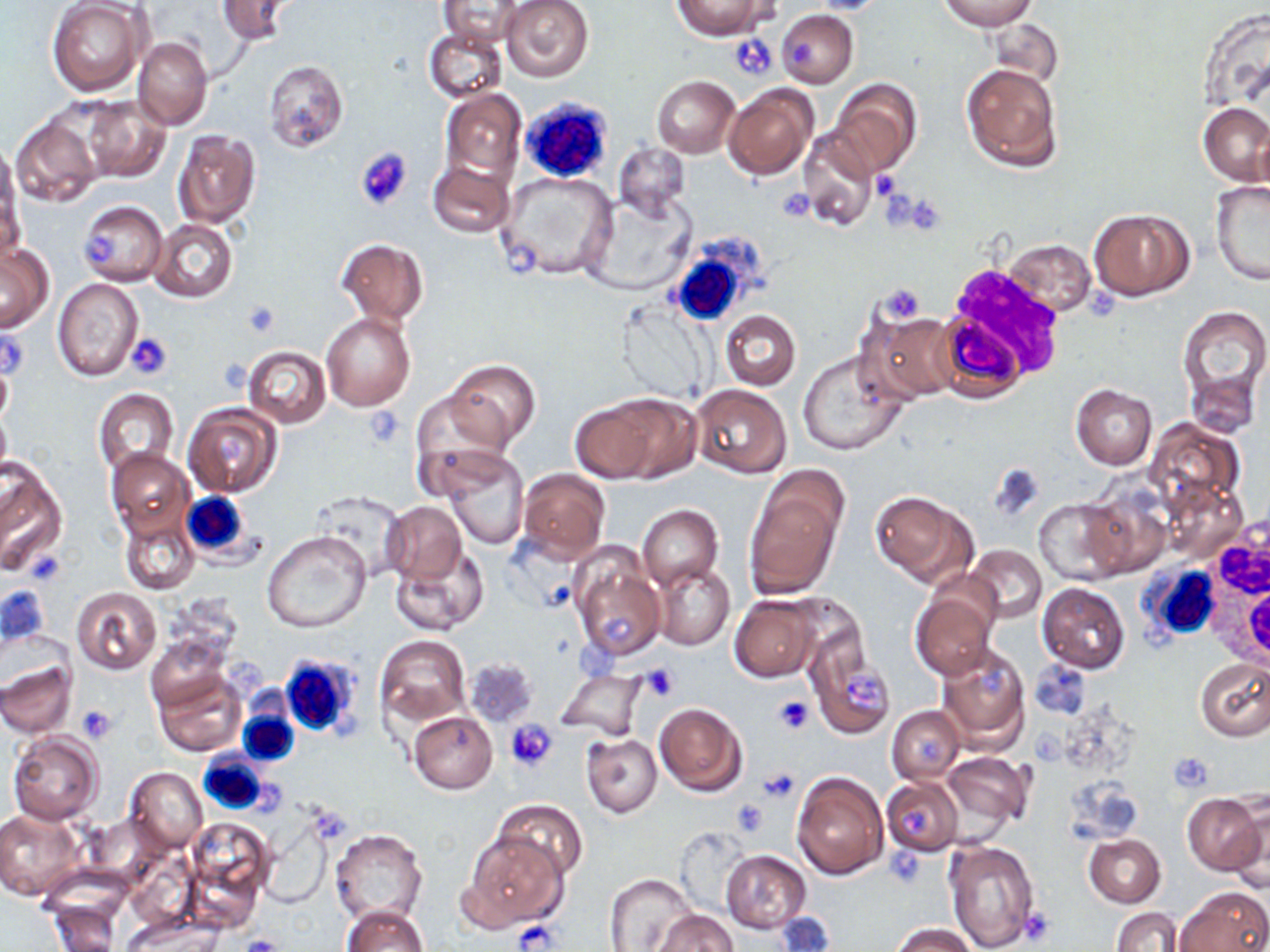
{
  "slide_level_diagnosis": "no evidence of blood parasites",
  "uninfected_red_blood_cell_locations": "approximate bounding boxes as [x1, y1, x2, y2] in pixels: [216, 0, 298, 44], [438, 0, 529, 48], [500, 0, 594, 83], [673, 0, 771, 39], [938, 0, 1036, 30], [805, 1, 896, 15], [47, 2, 149, 96], [776, 10, 858, 88], [987, 17, 1063, 88], [423, 28, 508, 102], [132, 38, 212, 129], [263, 60, 348, 152], [962, 63, 1062, 173], [651, 75, 739, 158], [831, 79, 921, 175], [723, 84, 817, 180], [439, 88, 527, 185], [77, 95, 170, 184], [1199, 104, 1270, 186], [10, 113, 102, 210], [796, 125, 879, 231], [171, 129, 260, 228], [0, 138, 19, 232], [613, 143, 691, 221], [428, 161, 514, 238], [497, 172, 619, 282], [1210, 180, 1270, 286], [1, 183, 24, 267], [583, 193, 695, 296], [78, 201, 166, 285], [1089, 208, 1193, 301], [148, 218, 238, 303], [337, 239, 428, 325], [1003, 239, 1097, 316], [1, 242, 54, 332], [52, 277, 143, 382], [615, 301, 714, 404], [1178, 305, 1270, 412], [860, 309, 964, 403], [321, 311, 416, 412], [719, 311, 800, 389], [242, 345, 330, 428], [797, 351, 908, 456], [0, 358, 12, 431], [444, 359, 539, 449], [1070, 383, 1156, 469], [690, 385, 792, 479], [92, 389, 179, 475], [409, 392, 511, 497], [571, 394, 679, 484], [183, 402, 282, 498], [0, 409, 11, 476], [1146, 416, 1245, 513], [106, 448, 195, 541], [438, 448, 531, 549], [0, 464, 65, 575], [519, 468, 611, 560], [745, 477, 846, 598], [1159, 479, 1247, 566], [1081, 486, 1173, 580], [870, 491, 977, 588], [1034, 496, 1129, 586], [383, 502, 465, 584], [637, 504, 722, 592], [118, 506, 200, 596], [261, 530, 371, 634], [965, 545, 1047, 623], [391, 547, 490, 635], [571, 553, 665, 659], [652, 562, 734, 650], [1037, 583, 1130, 672], [71, 587, 161, 674], [911, 587, 997, 678], [729, 596, 820, 681], [374, 635, 470, 726], [804, 639, 896, 739], [935, 644, 1030, 754], [1196, 658, 1270, 740], [465, 659, 538, 726], [1029, 659, 1091, 719], [0, 663, 76, 739], [150, 666, 248, 758], [556, 668, 647, 740], [655, 703, 746, 796], [886, 706, 964, 784], [408, 711, 497, 793], [8, 732, 103, 825], [583, 734, 662, 817], [942, 751, 1035, 829], [124, 768, 208, 853], [792, 770, 888, 878], [881, 777, 963, 855], [1183, 792, 1267, 875], [493, 798, 588, 882], [1228, 801, 1270, 895], [0, 809, 85, 901], [259, 814, 333, 908], [184, 819, 274, 919], [331, 829, 427, 924], [460, 831, 564, 931], [1083, 833, 1164, 907], [943, 838, 1039, 952], [721, 850, 810, 933], [603, 873, 696, 952], [1176, 887, 1269, 952], [48, 902, 121, 951], [341, 904, 427, 952], [1111, 906, 1182, 952], [654, 910, 738, 952], [124, 913, 222, 951], [771, 913, 835, 952], [891, 922, 978, 952]",
  "modality": "optical microscopy",
  "stain": "May-Grünwald-Giemsa",
  "field_of_view": "one of a larger specimen",
  "platelet_locations": "approximate bounding boxes as [x1, y1, x2, y2] in pixels: [731, 34, 778, 80], [788, 34, 819, 70], [355, 146, 412, 212], [871, 171, 900, 201], [776, 188, 817, 220], [902, 194, 949, 235], [1084, 282, 1121, 321], [874, 285, 926, 325], [239, 300, 281, 338], [1, 328, 29, 381], [127, 332, 173, 380], [364, 408, 405, 448], [990, 465, 1044, 523], [24, 548, 66, 586], [597, 611, 635, 645], [574, 636, 619, 684], [975, 662, 1008, 700], [643, 666, 680, 701], [845, 674, 885, 707], [771, 695, 814, 736], [77, 706, 116, 742], [507, 719, 559, 771], [915, 733, 948, 764], [1168, 751, 1214, 793], [758, 769, 799, 801], [731, 797, 771, 834], [900, 805, 934, 833], [886, 847, 928, 888], [1017, 909, 1056, 946], [515, 921, 559, 950], [240, 934, 285, 952]",
  "preparation": "thin blood smear",
  "image_size": "1270×952 pixels",
  "white_blood_cell_locations": "approximate bounding boxes as [x1, y1, x2, y2] in pixels: [519, 97, 613, 186], [670, 242, 758, 327], [181, 491, 255, 561], [1205, 515, 1270, 653], [1139, 556, 1219, 647], [278, 652, 366, 741], [238, 710, 300, 768], [197, 751, 270, 817]",
  "magnification": "1000x"
}